State which parasite is depicted.
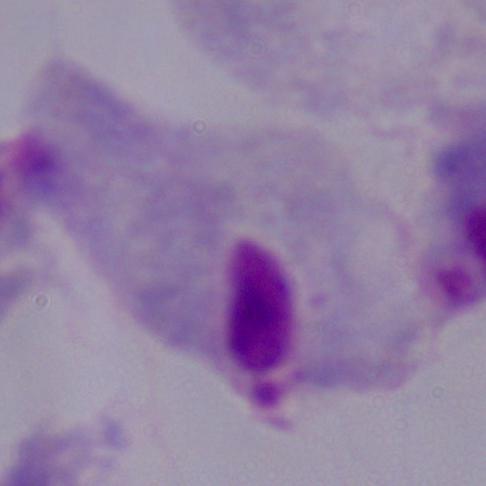

This is a trichomonad.

Captured at 1000x magnification. Photomicrograph.